State the blood parasite species.
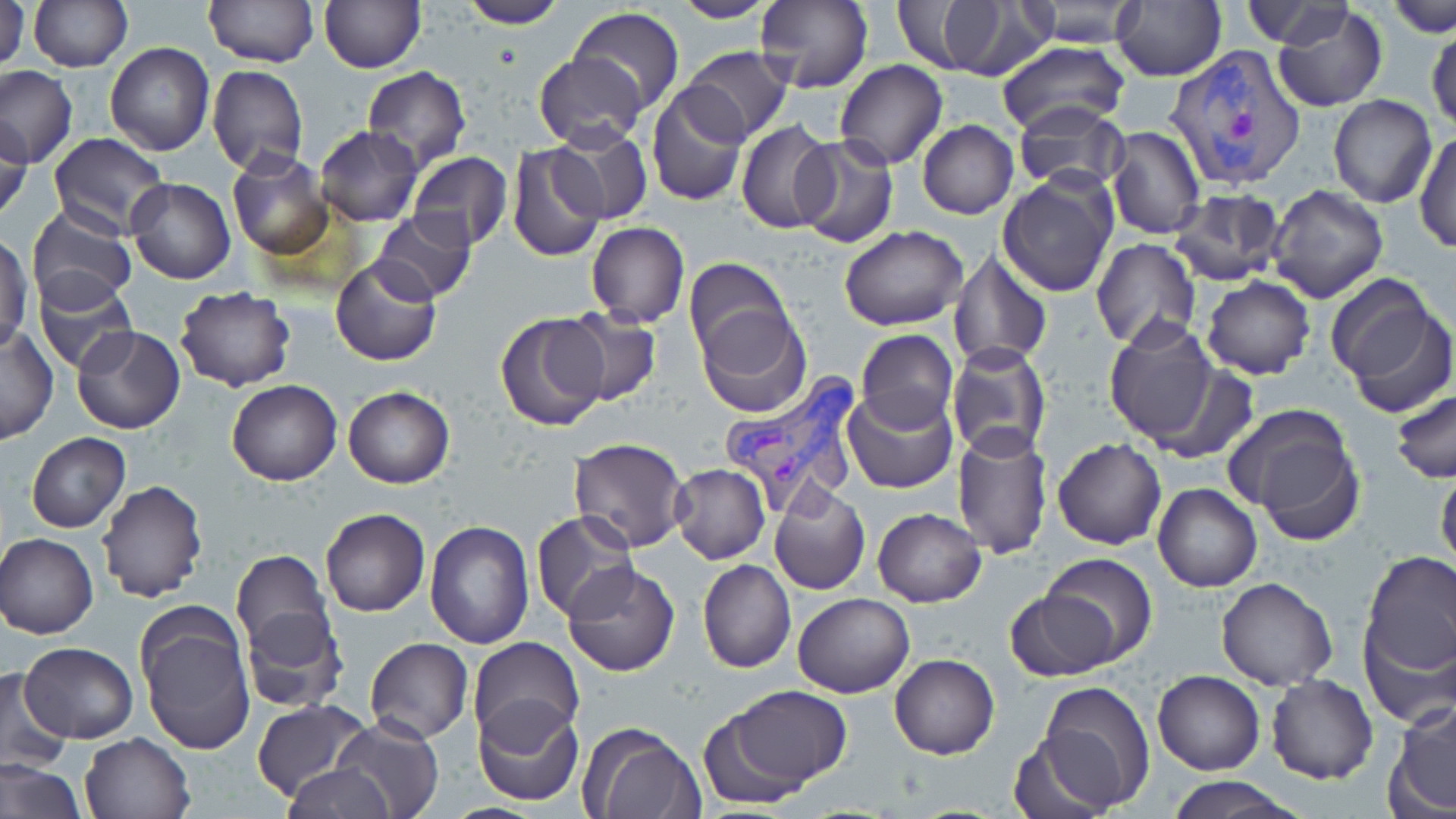

Plasmodium vivax.

modality = light microscopy
image size = 1456×819 pixels
field of view = single
stain = May-Grünwald-Giemsa
uninfected red blood cell locations = approximate bounding boxes as (x1,y1)-(x2,y2) corner pairs in pixels: (0,0)-(29,70), (457,0)-(566,28), (668,0)-(778,23), (756,0)-(872,93), (888,0)-(1043,80), (1011,0)-(1145,49), (1111,0)-(1227,83), (203,1)-(319,68), (1239,1)-(1358,48), (1382,1)-(1456,36), (28,2)-(132,72), (320,2)-(425,71), (1271,6)-(1389,112), (568,8)-(685,119), (1429,19)-(1456,132), (995,39)-(1132,142), (105,42)-(214,156), (679,44)-(794,145), (534,53)-(646,151), (834,60)-(948,170), (206,63)-(309,176), (0,65)-(77,169), (362,67)-(472,169), (647,84)-(750,207), (1328,95)-(1436,208), (1011,103)-(1131,195), (0,115)-(32,220), (734,120)-(836,234), (917,120)-(1018,220), (314,126)-(422,226), (549,126)-(653,225), (1105,126)-(1206,241), (1413,130)-(1455,254), (48,131)-(170,239), (791,134)-(899,248), (507,143)-(607,263), (407,150)-(514,249), (226,151)-(335,261), (998,171)-(1117,297), (125,177)-(235,285), (1267,184)-(1388,303), (1167,190)-(1287,287), (27,206)-(137,314), (371,207)-(477,304), (585,221)-(689,327), (839,225)-(967,330), (0,233)-(33,353), (1090,238)-(1202,350), (946,249)-(1054,371), (330,255)-(443,367), (684,256)-(795,371), (34,275)-(138,374), (1201,277)-(1316,380), (1329,281)-(1454,416), (175,286)-(296,391), (693,306)-(810,418), (556,308)-(662,409), (494,310)-(612,431), (1103,317)-(1221,447), (71,324)-(185,434), (1,327)-(57,445), (855,328)-(958,433), (945,342)-(1053,461), (228,380)-(342,485), (342,387)-(454,488), (842,387)-(957,494), (1391,388)-(1456,484), (1225,405)-(1365,539), (951,426)-(1055,560), (25,432)-(131,533), (567,438)-(690,553), (1052,438)-(1166,550), (669,464)-(770,565), (1436,465)-(1456,576), (97,480)-(209,603), (1153,483)-(1260,592), (768,484)-(871,595), (320,506)-(430,616), (872,507)-(986,605), (531,511)-(641,625), (424,520)-(535,649), (1,533)-(99,639), (230,548)-(332,653), (1358,550)-(1456,681), (1040,552)-(1159,666), (699,559)-(797,673), (562,563)-(680,677), (1216,577)-(1338,691), (1003,587)-(1122,682), (793,592)-(914,699), (135,606)-(257,756), (240,607)-(347,712), (1361,623)-(1455,728), (365,637)-(473,744), (467,637)-(584,750), (20,642)-(138,744), (888,653)-(1000,758), (0,670)-(73,772), (1153,671)-(1263,775), (1267,674)-(1378,785), (1032,680)-(1157,813), (719,686)-(852,794), (473,698)-(584,807), (251,699)-(371,803), (1386,700)-(1456,817), (330,715)-(443,819), (578,722)-(706,819), (79,732)-(195,819), (1007,732)-(1116,819), (0,759)-(85,819), (281,764)-(396,818), (1163,775)-(1306,819)
magnification = 1000x
preparation = thin blood smear
Plasmodium vivax-infected red blood cell locations = approximate bounding boxes as (x1,y1)-(x2,y2) corner pairs in pixels: (1169,43)-(1306,189), (721,375)-(865,516)